Name the cell type shown.
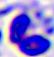
This is a leukocyte.

Summary:
  - Magnification: 400x
  - Modality: photomicrograph